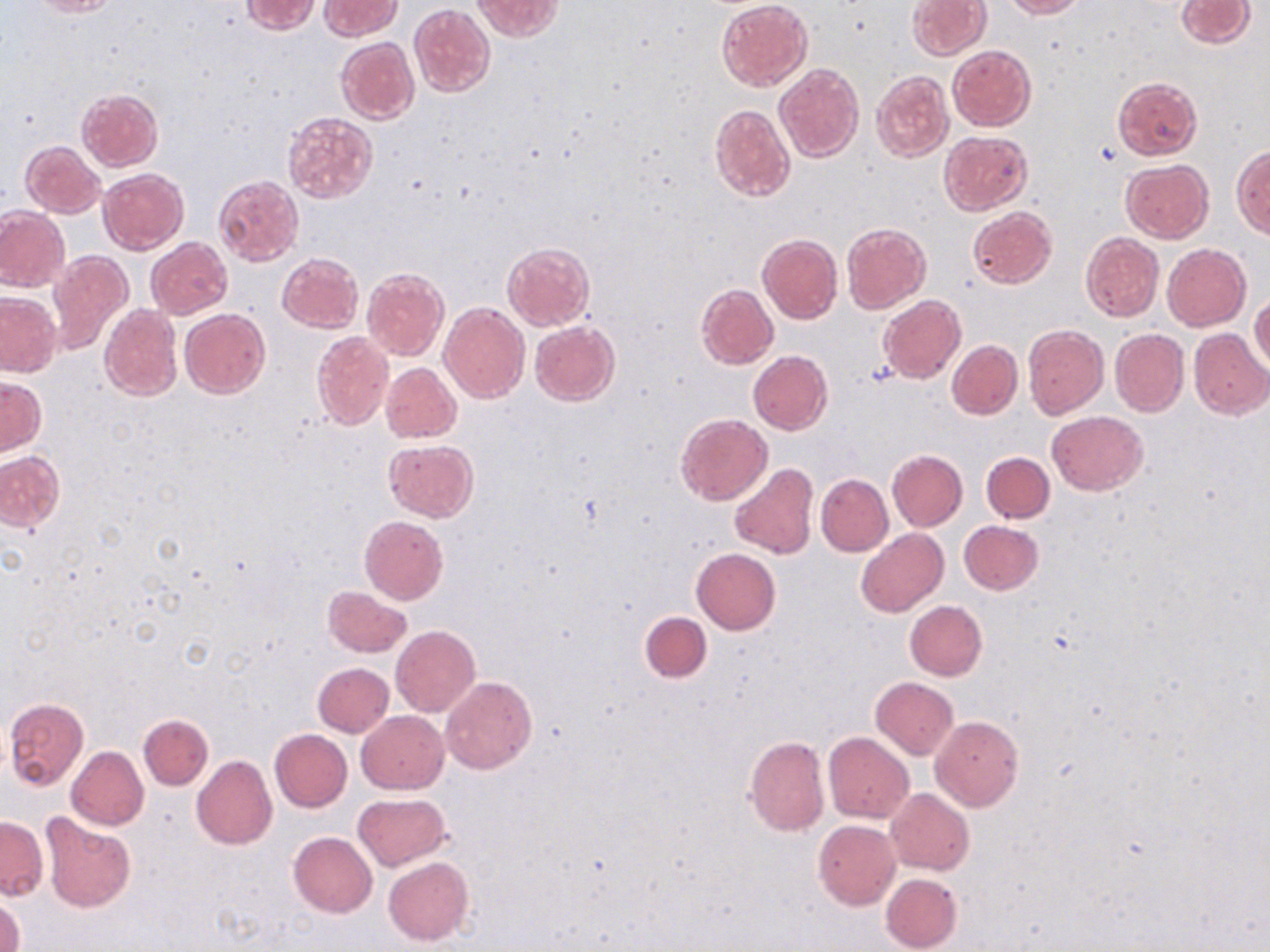
Summary:
  - Coordinate format: approximate bounding boxes as (x1, y1, x2, y2) in pixels
  - Uninfected red blood cell locations: (28, 0, 118, 17), (320, 0, 402, 39), (471, 0, 562, 41), (717, 0, 811, 90), (907, 0, 990, 61), (1000, 0, 1084, 18), (1175, 0, 1254, 48), (241, 1, 322, 34), (409, 4, 494, 98), (335, 37, 419, 125), (947, 45, 1036, 130), (774, 64, 863, 164), (871, 71, 953, 161), (1113, 76, 1201, 160), (76, 89, 164, 171), (710, 104, 795, 202), (283, 112, 378, 202), (939, 130, 1032, 215), (20, 140, 104, 218), (1231, 146, 1270, 239), (1120, 160, 1213, 243), (97, 168, 190, 254), (213, 176, 304, 266), (0, 207, 70, 291), (967, 207, 1056, 289), (841, 222, 930, 313), (1081, 232, 1163, 320), (757, 235, 843, 324), (146, 238, 233, 319), (501, 241, 595, 330), (1163, 244, 1250, 331), (48, 251, 134, 357), (277, 252, 364, 332), (361, 269, 448, 360), (696, 283, 778, 369), (0, 292, 61, 376), (1250, 294, 1270, 373), (877, 296, 966, 383), (438, 304, 530, 405), (99, 305, 181, 401), (180, 308, 270, 398), (530, 319, 619, 405), (1022, 324, 1110, 419), (1110, 329, 1189, 416), (1188, 329, 1269, 420), (311, 331, 393, 429), (947, 340, 1022, 418), (748, 351, 832, 435), (380, 362, 462, 443), (0, 377, 45, 456), (1046, 411, 1149, 495), (675, 412, 772, 506), (384, 440, 478, 521), (886, 449, 967, 531), (0, 450, 64, 533), (981, 452, 1054, 523), (729, 462, 818, 559), (815, 473, 892, 556), (359, 516, 448, 605), (958, 520, 1043, 595), (856, 528, 948, 617), (691, 548, 780, 634), (323, 586, 412, 658), (904, 600, 987, 681), (639, 611, 712, 683), (391, 626, 480, 717), (313, 662, 394, 736), (440, 676, 536, 774), (871, 677, 959, 759), (5, 697, 89, 789), (356, 710, 448, 794), (139, 714, 213, 790), (930, 716, 1024, 812), (269, 729, 352, 812), (823, 732, 914, 823), (744, 736, 829, 836), (66, 746, 148, 830), (191, 755, 276, 849), (885, 788, 974, 874), (352, 793, 451, 871), (41, 812, 136, 913), (0, 817, 48, 900), (813, 819, 901, 910), (288, 832, 377, 917), (383, 856, 474, 946), (881, 873, 963, 952), (1, 895, 24, 952)
  - Slide-level diagnosis: no evidence of blood parasites
  - Image size: 1270×952 pixels
  - Magnification: 1000x
  - Preparation: thin blood film
  - Field of view: single
  - Modality: light microscopy
  - Stain: May-Grünwald-Giemsa